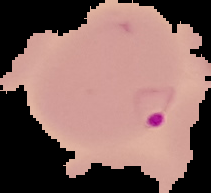
Summary:
  - Image type: segmented cell region on a black background
  - Preparation: thin blood film
  - Malaria status: parasitized
  - Image size: 211×193 pixels